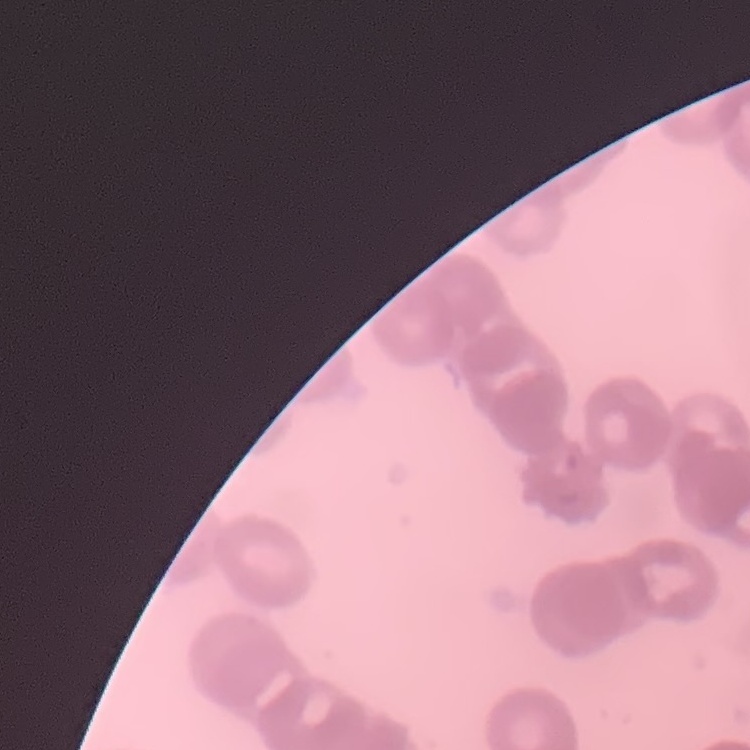 The erythrocytes exhibit rouleaux formation. Field's or Giemsa stain. One tile cut from a larger photomicrograph. Thin blood smear.